Give the preparation type.
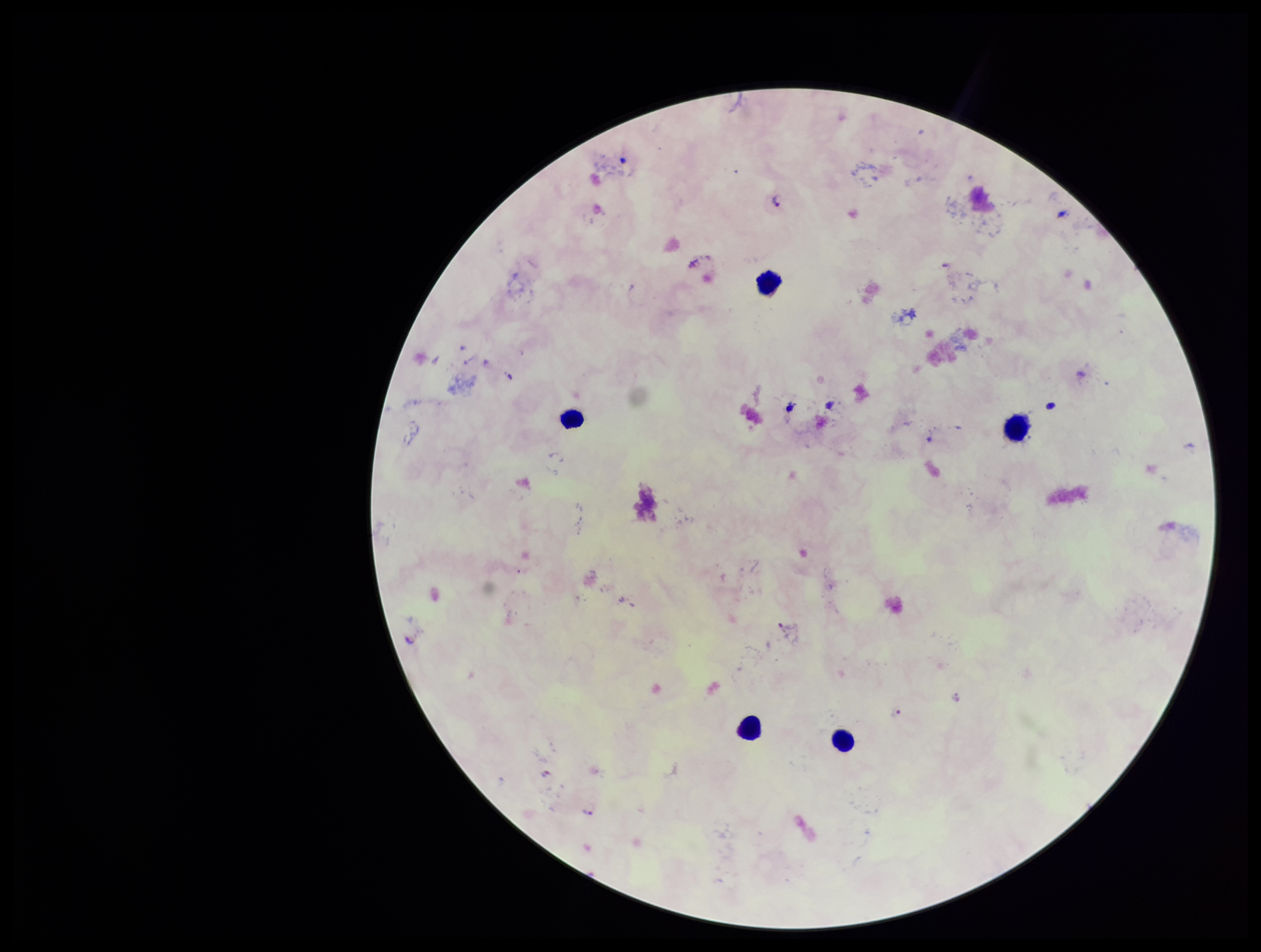

Thick.

Summary:
  - Capture: smartphone photograph through the microscope eyepiece
  - Leukocyte count: 5
  - Plasmodium parasites: detected
  - Image size: 1261×952 pixels
  - Species reported for this patient: Plasmodium falciparum
  - Field of view: single
  - Patient malaria status: positive
  - Stain: Giemsa
  - Parasite count: 4